Outline each Plasmodium falciparum parasite and classify it by life-cycle stage.
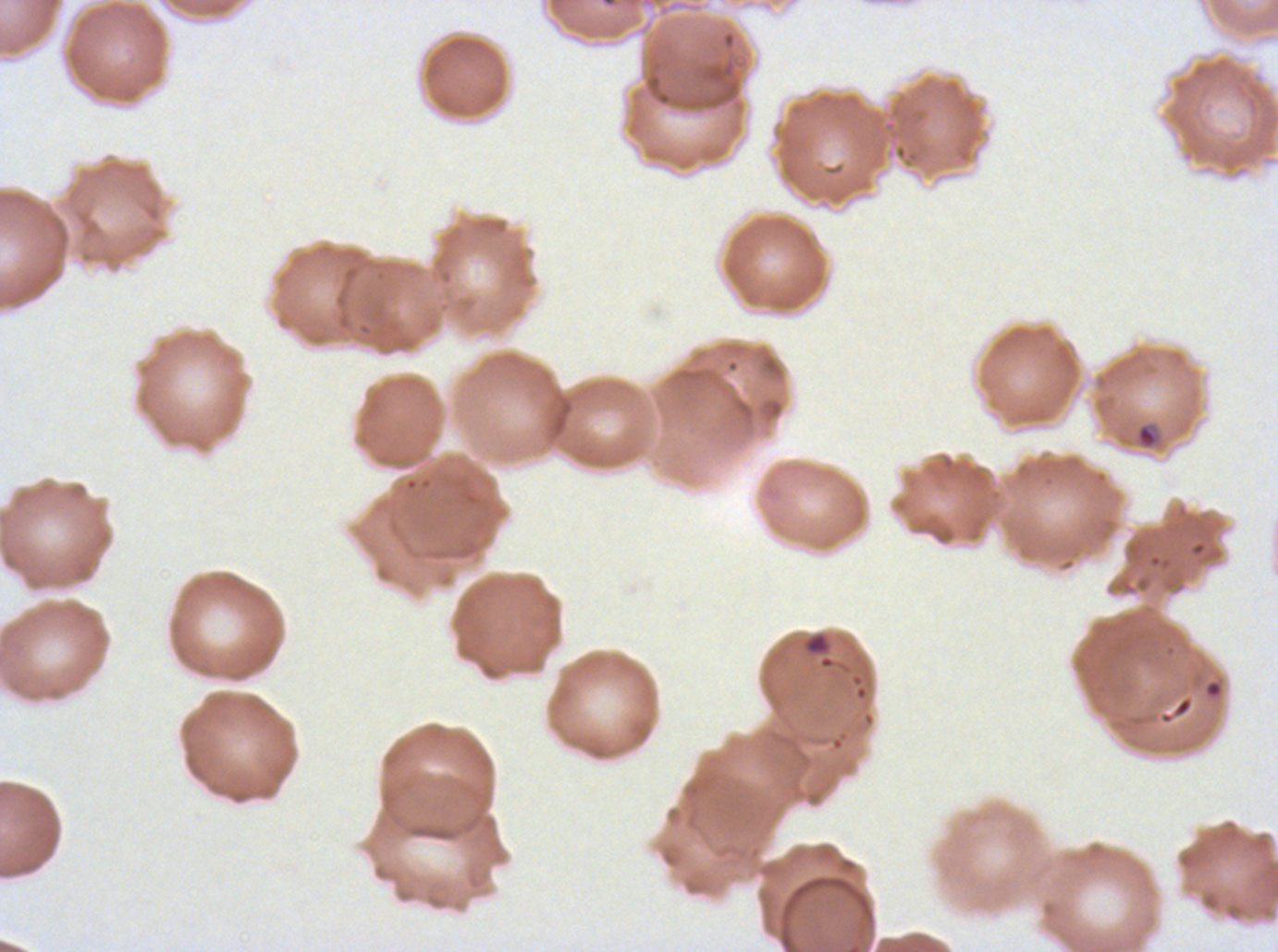
Approximate bounding boxes as [x1, y1, x2, y2] in pixels.
Rings: [1136, 422, 1159, 449].
No late-ring/early-trophozoite forms, mid trophozoites, late trophozoites, early schizonts, late schizonts, segmenters, or gametocytes observed.

Debris locations: [805, 632, 829, 654]. Image is 1278×952 pixels. One sub-image of a larger composite. Plasmodium falciparum from a patient in The Gambia, cultured ex vivo for 24 to 48 hours. Giemsa-stained preparation. Thin blood film.